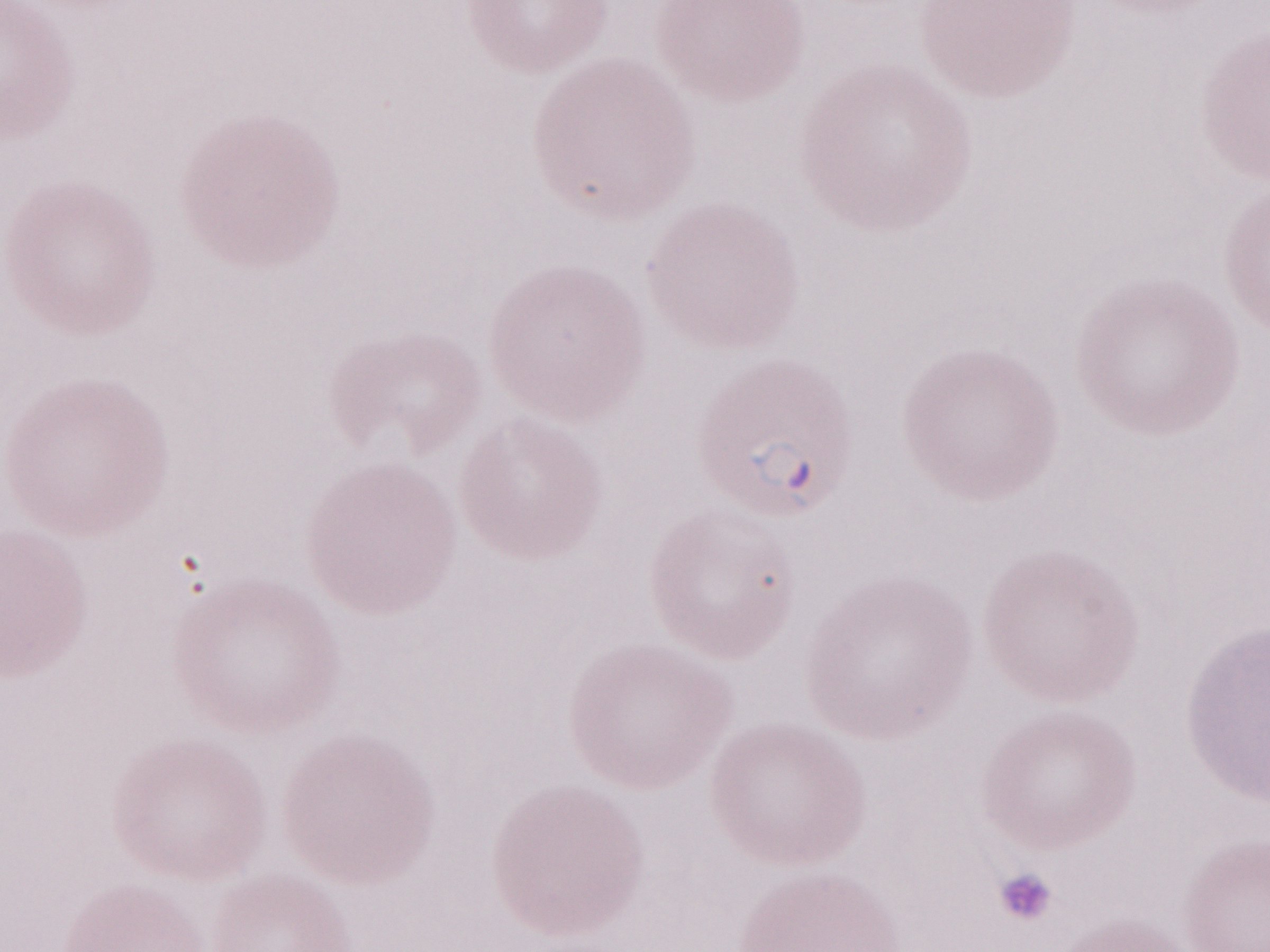

May-Grünwald-Giemsa-stained preparation. Single field of view. Thin blood smear. Olympus BX43 microscope, Olympus DP73 camera. Patient-level malaria diagnosis: positive. Image is 1270×952 pixels. 1,000x magnification.